Report the malaria status.
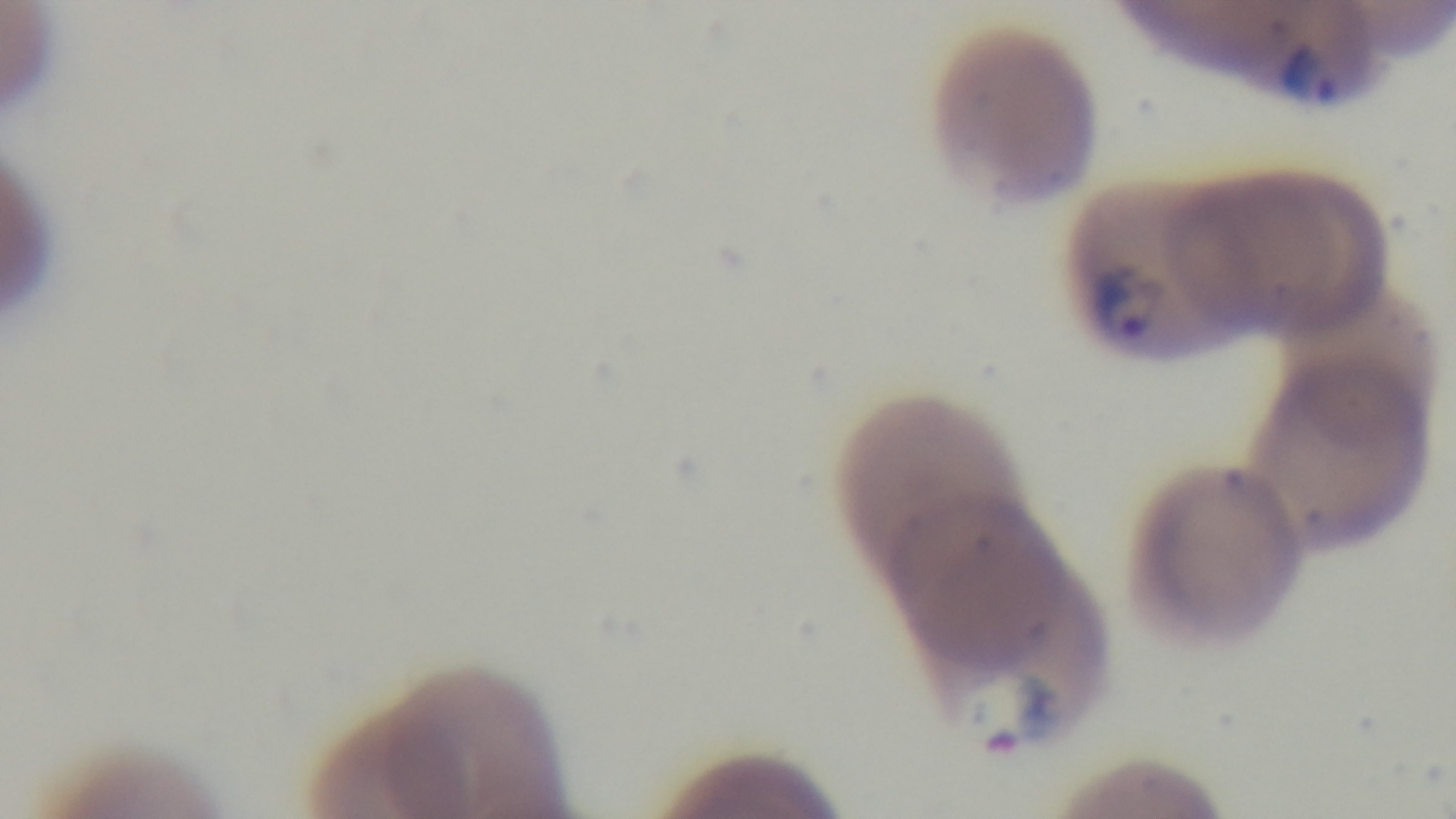
Positive.

capture = mounted 4K digital camera
field of view = single
modality = light microscopy
stain = Giemsa
preparation = thin smear
objective = 100x oil immersion